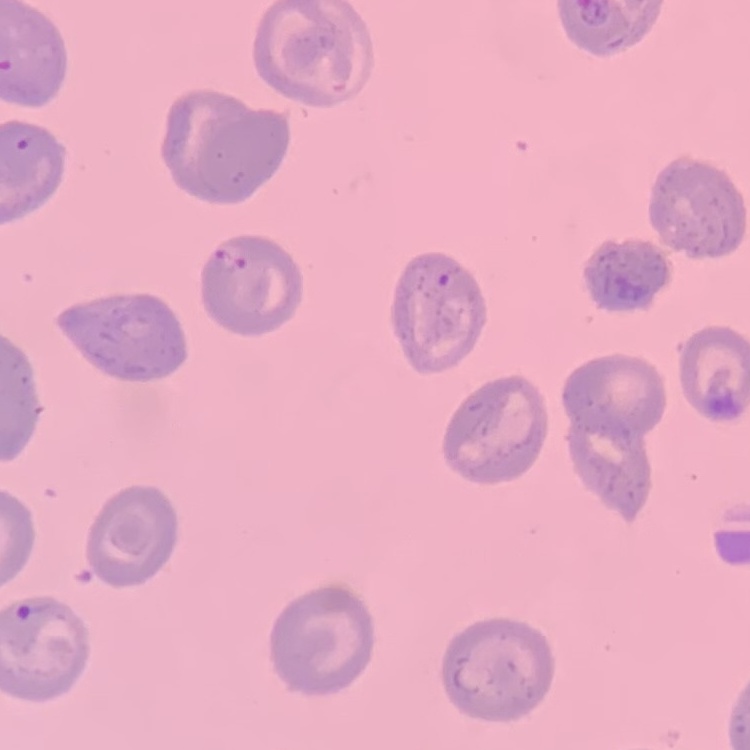
Summary:
  - Erythrocyte morphology: no rouleaux formation
  - Stain: Field's or Giemsa
  - Preparation: thin blood smear
  - Image type: one tile cut from a larger photomicrograph